Give the extent of all uninfected red blood cells.
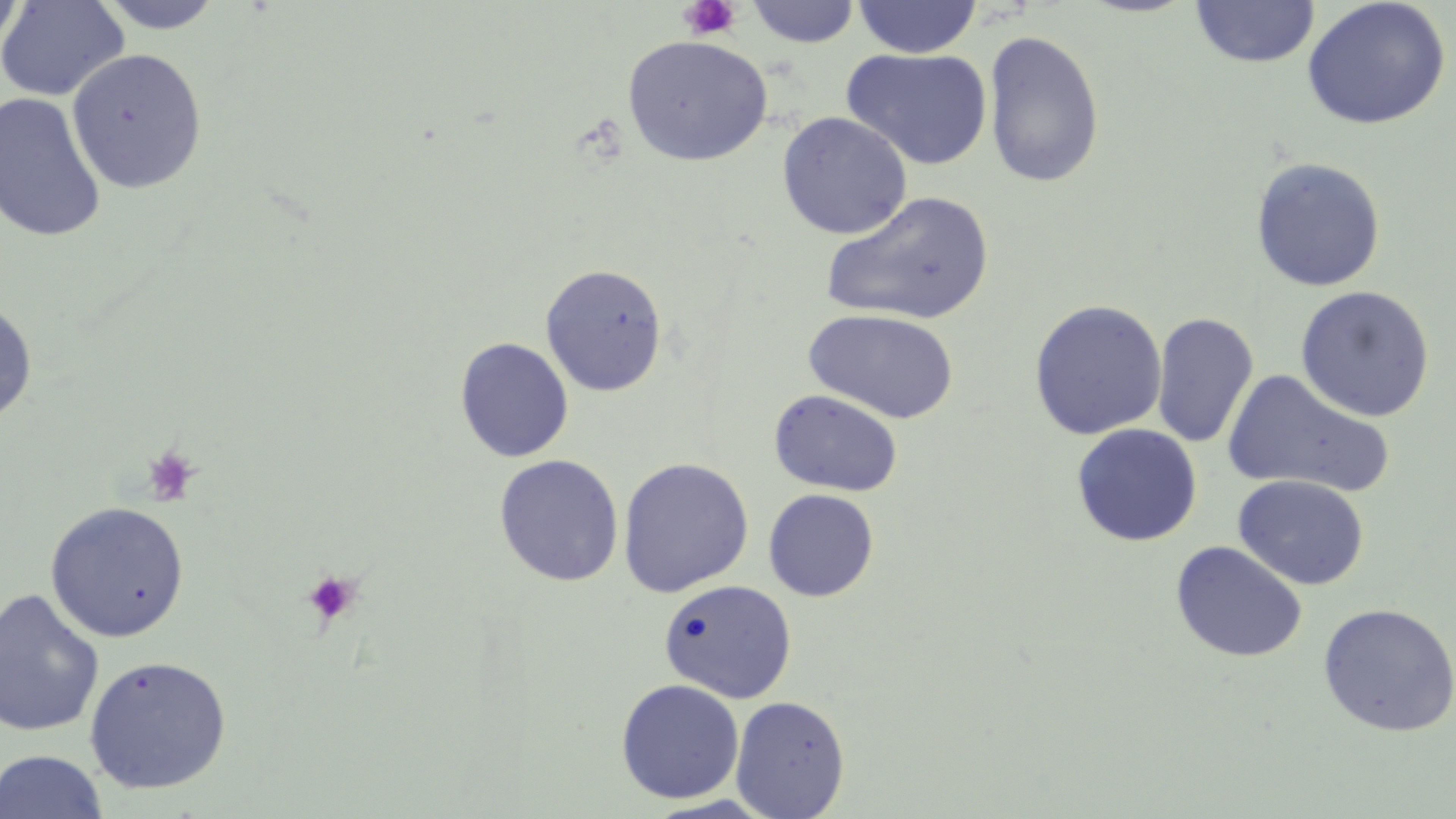

Approximate bounding boxes as (x1,y1)-(x2,y2) corner pairs in pixels.
Uninfected red blood cells: (0,0)-(129,102), (0,0)-(26,59), (94,0)-(226,34), (852,0)-(982,59), (1301,0)-(1452,130), (746,1)-(861,47), (1190,1)-(1320,68), (983,28)-(1105,189), (622,35)-(773,167), (66,47)-(207,194), (841,47)-(992,171), (0,91)-(107,243), (776,111)-(913,240), (1250,157)-(1386,292), (820,191)-(995,326), (540,263)-(668,397), (1294,285)-(1435,422), (0,299)-(38,428), (1028,299)-(1167,441), (803,308)-(960,424), (1151,311)-(1259,448), (454,337)-(574,463), (1222,369)-(1394,500), (768,389)-(904,497), (1071,423)-(1202,547), (494,454)-(624,587), (618,457)-(754,597), (1234,475)-(1369,590), (763,489)-(879,602), (44,501)-(190,642), (1170,541)-(1309,663), (659,578)-(797,703), (0,587)-(105,738), (1317,603)-(1456,736), (83,654)-(233,795), (615,678)-(745,804), (730,695)-(850,818), (0,750)-(109,819).

Platelet locations: (678,0)-(742,40), (141,445)-(202,506), (301,569)-(362,627). Slide-level diagnosis: no evidence of blood parasites. Optical microscopy. Image is 1456×819 pixels. Thin blood film. May-Grünwald-Giemsa-stained preparation. Captured at 1000x magnification. One field of a larger specimen.